Name the blood parasite species.
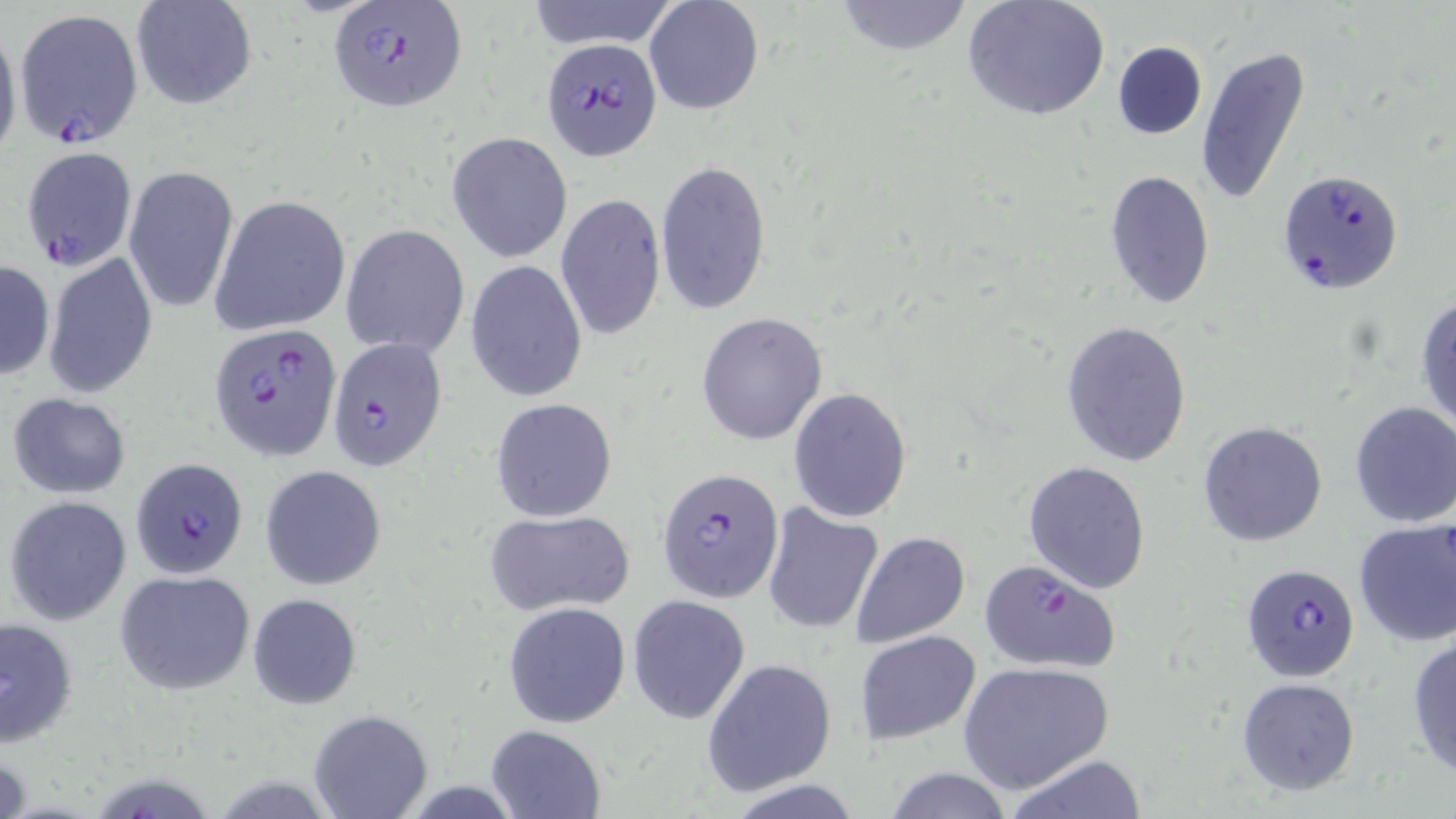
Plasmodium falciparum.

{
  "stain": "May-Grünwald-Giemsa",
  "uninfected_red_blood_cell_locations": "approximate bounding boxes as named x1/y1/x2/y2 corners in pixels: (x1=526, y1=0, x2=679, y2=51), (x1=643, y1=0, x2=764, y2=117), (x1=831, y1=0, x2=976, y2=57), (x1=961, y1=0, x2=1111, y2=123), (x1=130, y1=2, x2=257, y2=110), (x1=0, y1=18, x2=22, y2=171), (x1=1111, y1=41, x2=1207, y2=140), (x1=1196, y1=47, x2=1311, y2=205), (x1=446, y1=131, x2=573, y2=263), (x1=654, y1=159, x2=772, y2=315), (x1=123, y1=164, x2=238, y2=313), (x1=1102, y1=171, x2=1216, y2=310), (x1=555, y1=194, x2=666, y2=342), (x1=212, y1=195, x2=351, y2=336), (x1=341, y1=224, x2=470, y2=358), (x1=45, y1=253, x2=159, y2=400), (x1=465, y1=258, x2=588, y2=403), (x1=1, y1=260, x2=54, y2=379), (x1=1414, y1=294, x2=1456, y2=437), (x1=696, y1=312, x2=828, y2=446), (x1=1059, y1=320, x2=1193, y2=468), (x1=788, y1=387, x2=912, y2=523), (x1=6, y1=392, x2=133, y2=499), (x1=489, y1=399, x2=618, y2=521), (x1=1348, y1=401, x2=1456, y2=529), (x1=1197, y1=420, x2=1329, y2=547), (x1=1022, y1=461, x2=1151, y2=594), (x1=259, y1=466, x2=387, y2=590), (x1=4, y1=494, x2=132, y2=627), (x1=762, y1=501, x2=884, y2=634), (x1=483, y1=511, x2=634, y2=618), (x1=1352, y1=519, x2=1456, y2=648), (x1=848, y1=530, x2=972, y2=647), (x1=114, y1=569, x2=256, y2=696), (x1=626, y1=593, x2=751, y2=726), (x1=248, y1=594, x2=362, y2=708), (x1=503, y1=601, x2=631, y2=727), (x1=1, y1=614, x2=79, y2=749), (x1=855, y1=630, x2=981, y2=744), (x1=1406, y1=634, x2=1456, y2=779), (x1=701, y1=657, x2=838, y2=796), (x1=958, y1=661, x2=1113, y2=794), (x1=1236, y1=676, x2=1362, y2=797), (x1=308, y1=707, x2=433, y2=819), (x1=485, y1=724, x2=607, y2=819), (x1=1004, y1=754, x2=1148, y2=819), (x1=882, y1=767, x2=1019, y2=819)",
  "magnification": "1000x",
  "plasmodium_falciparum_infected_red_blood_cell_locations": "approximate bounding boxes as named x1/y1/x2/y2 corners in pixels: (x1=326, y1=2, x2=468, y2=114), (x1=14, y1=9, x2=143, y2=148), (x1=540, y1=35, x2=663, y2=161), (x1=20, y1=147, x2=137, y2=272), (x1=1277, y1=168, x2=1404, y2=295), (x1=210, y1=324, x2=341, y2=460), (x1=327, y1=338, x2=448, y2=471), (x1=131, y1=457, x2=248, y2=579), (x1=656, y1=466, x2=784, y2=602), (x1=978, y1=559, x2=1123, y2=674), (x1=1240, y1=561, x2=1360, y2=682)",
  "image_size": "1456×819 pixels",
  "field_of_view": "single",
  "modality": "optical microscopy",
  "preparation": "thin blood film"
}